Point out each Plasmodium parasite.
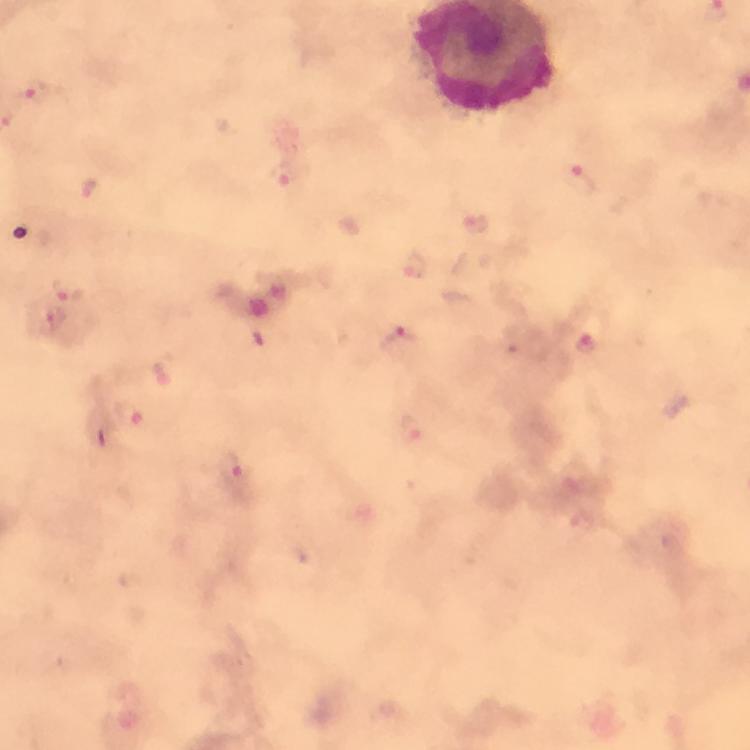
Approximate centers as {x, y} in pixels.
Plasmodium parasites: {32, 89}, {281, 177}, {578, 178}, {88, 190}, {475, 224}, {416, 265}, {68, 289}, {53, 320}, {400, 338}, {586, 342}, {131, 415}, {414, 428}, {230, 472}.

Image is 750×750 pixels. 100x magnification. Photographed with a smartphone mounted on the microscope. From a diagnostic examination for malaria. Thick blood film. Giemsa-stained preparation. Immersion oil was used. A crop from one field of view.